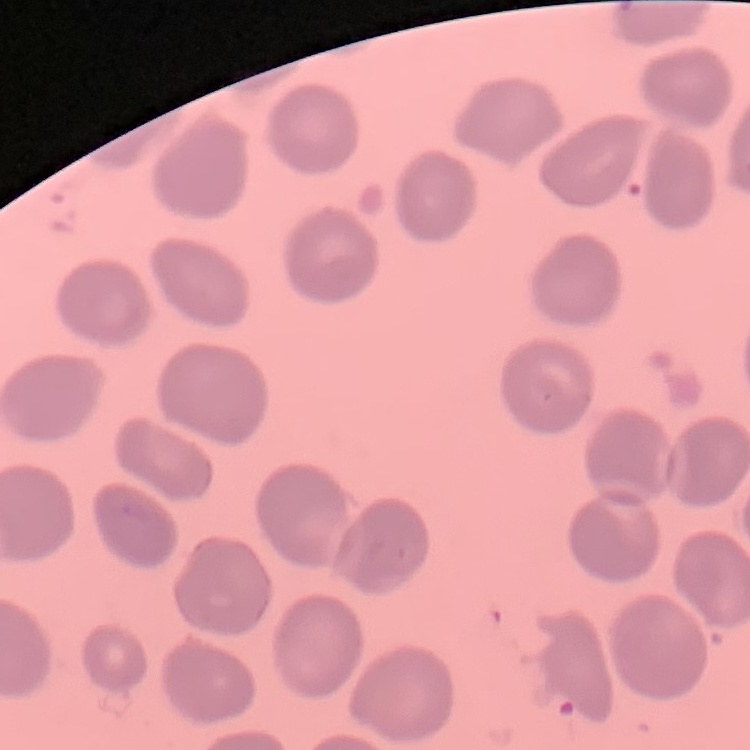

red blood cell morphology = no rouleaux formation
image type = square crop of a larger photomicrograph
preparation = thin blood smear
stain = Field's or Giemsa